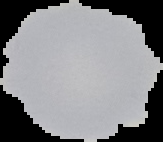

Summary:
  - Image type: cell region segmented out of the field of view; surrounding area masked to black
  - Image size: 163×142 pixels
  - Preparation: thin blood film
  - Result: negative for Plasmodium parasites